Comment on the morphology of the red blood cells.
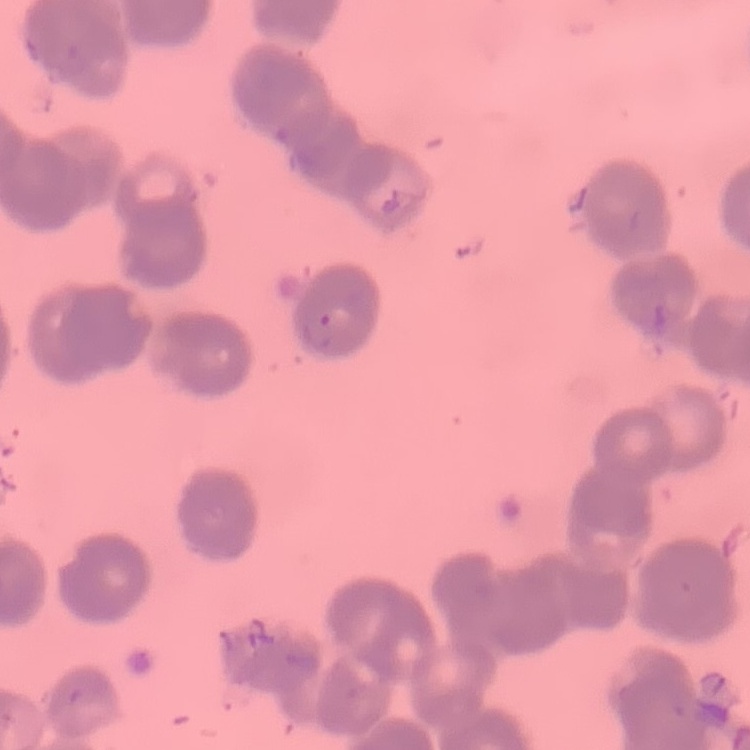
Rouleaux formation.

Summary:
  - Image type: one tile cut from a larger photomicrograph
  - Stain: Field's or Giemsa
  - Preparation: thin blood smear